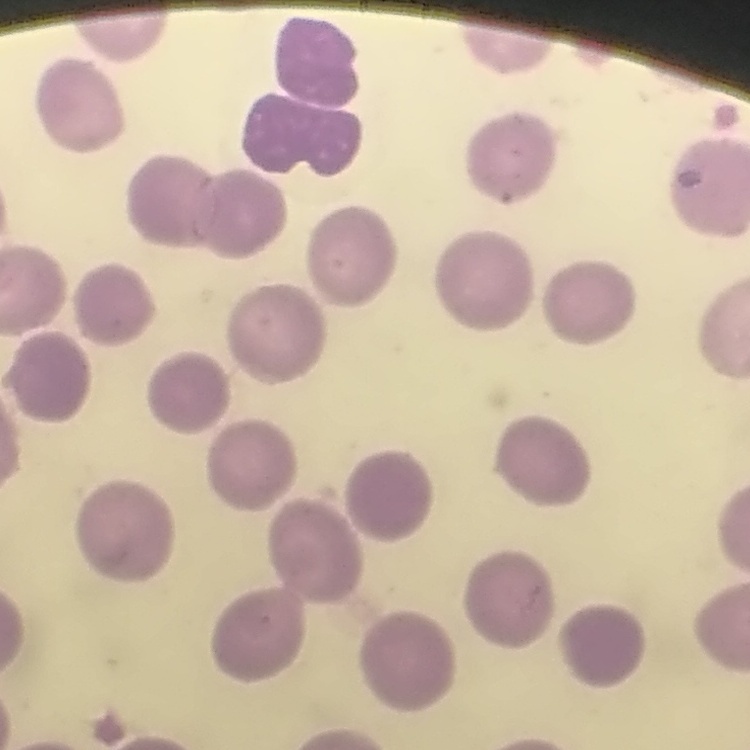

erythrocyte_morphology: no rouleaux formation
stain: Field's or Giemsa
image_type: one tile cut from a larger photomicrograph
preparation: thin blood smear